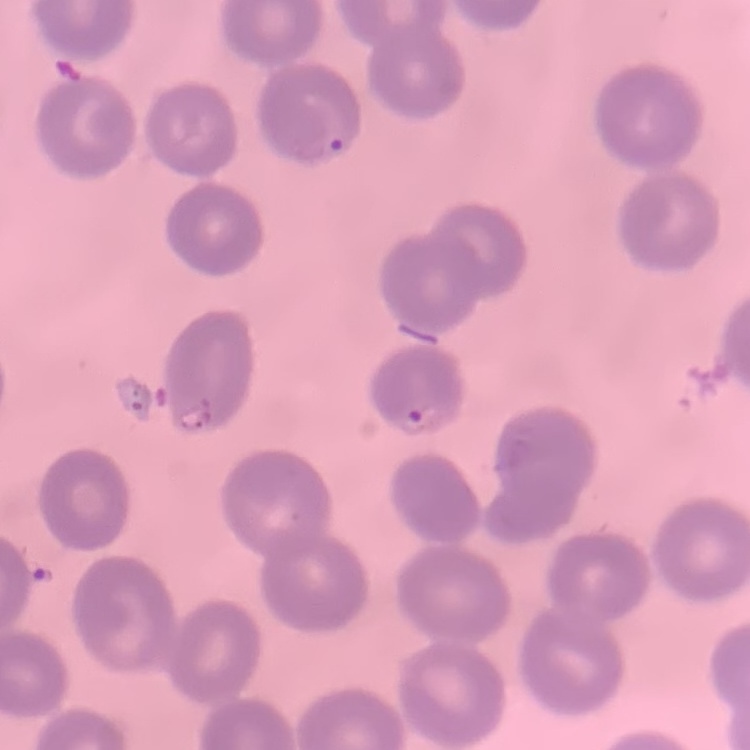

erythrocyte_morphology: no rouleaux formation
image_type: square crop of a larger photomicrograph
preparation: thin blood film
stain: Field's or Giemsa